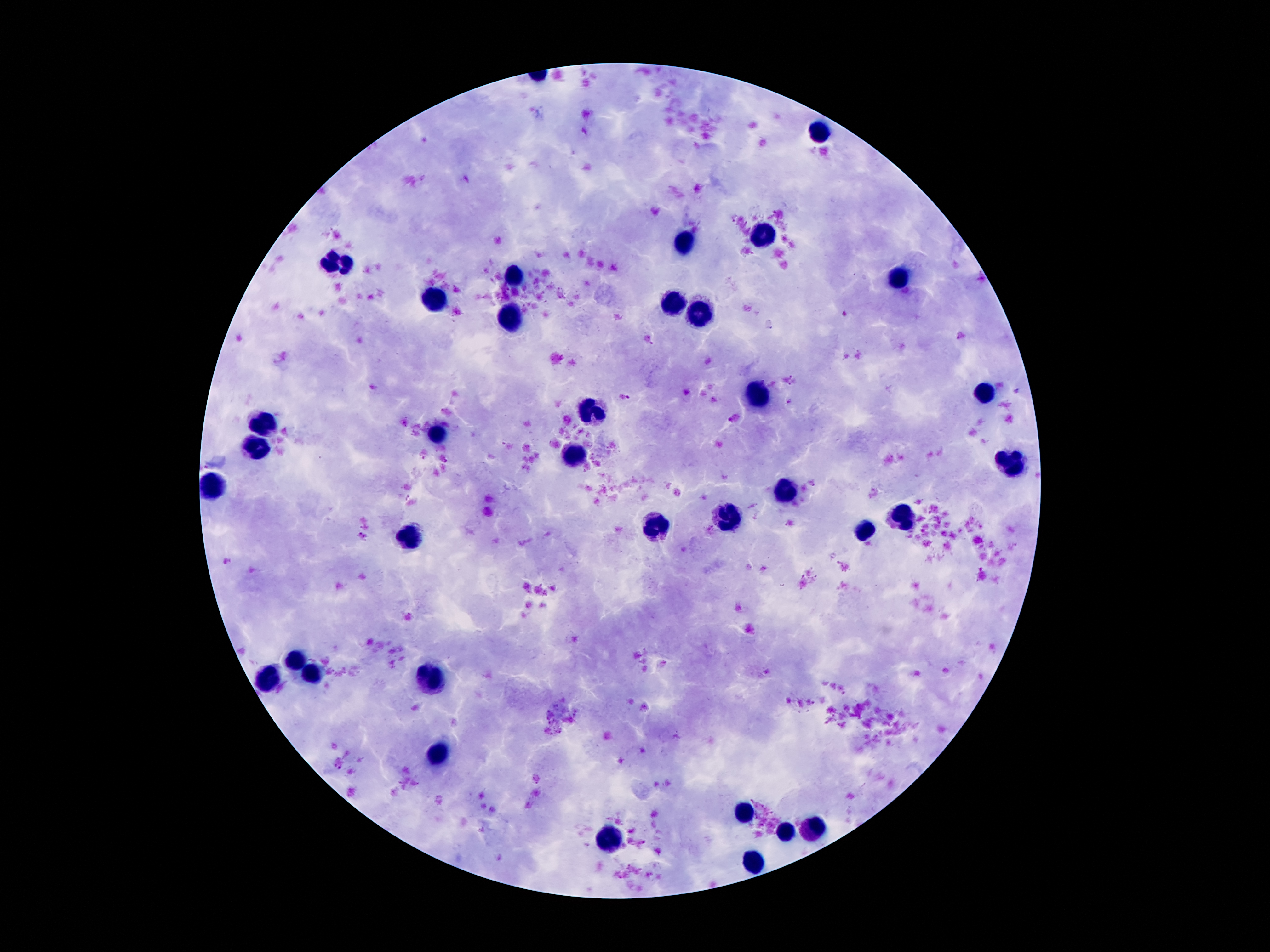

Approximate centers as (x, y) in pixels. Leukocyte locations: (814, 133), (762, 236), (680, 246), (338, 266), (897, 279), (515, 281), (437, 301), (674, 304), (697, 318), (510, 326), (984, 393), (756, 397), (592, 410), (265, 420), (437, 437), (253, 451), (574, 457), (1012, 461), (214, 486), (783, 488), (902, 517), (728, 518), (654, 527), (865, 529), (412, 535), (296, 660), (312, 672), (267, 674), (425, 680), (437, 754), (746, 813), (812, 830), (787, 832), (611, 839), (750, 861). Plasmodium parasite locations: (958, 336), (792, 380), (628, 397), (790, 402), (733, 418), (363, 536), (338, 767). Thick blood smear. Giemsa stain. Patient malaria status: infected with Plasmodium falciparum. 100x magnification. One field from this slide. Image is 1270×952 pixels. Photographed through the microscope eyepiece with a smartphone camera.